Outline each blood parasite and name the species.
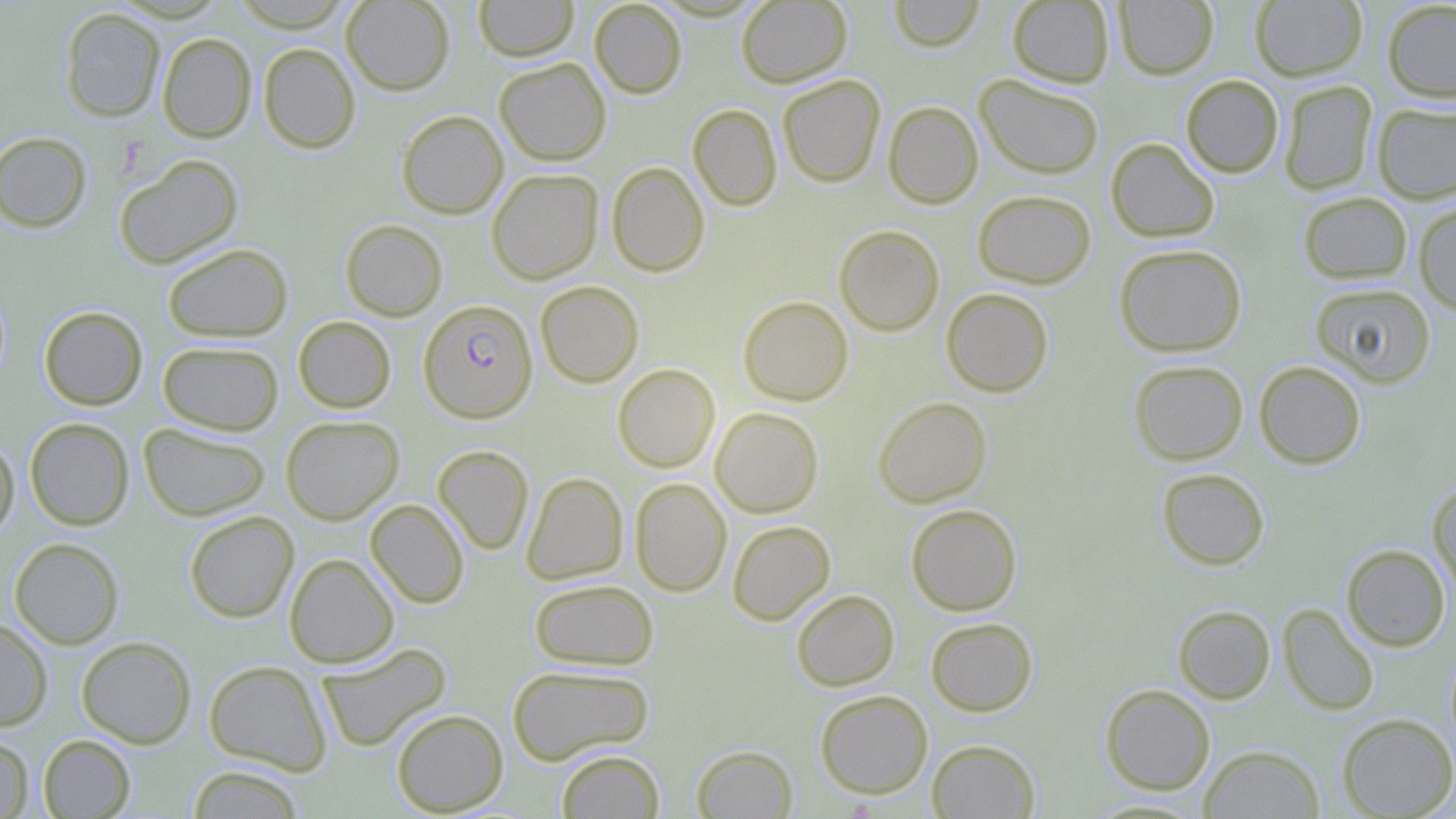

Approximate bounding boxes as named x1/y1/x2/y2 corners in pixels.
Plasmodium falciparum-infected red blood cells: (x1=418, y1=299, x2=537, y2=422).
No Plasmodium ovale, Plasmodium malariae, Plasmodium vivax, Babesia divergens, or Trypanosoma brucei observed.

Uninfected red blood cell locations: (x1=341, y1=0, x2=455, y2=95), (x1=474, y1=0, x2=579, y2=61), (x1=589, y1=0, x2=687, y2=98), (x1=736, y1=0, x2=852, y2=88), (x1=888, y1=0, x2=986, y2=52), (x1=1007, y1=0, x2=1114, y2=88), (x1=1114, y1=0, x2=1219, y2=79), (x1=1250, y1=0, x2=1367, y2=81), (x1=1381, y1=1, x2=1456, y2=103), (x1=60, y1=7, x2=165, y2=122), (x1=157, y1=33, x2=256, y2=142), (x1=259, y1=43, x2=360, y2=153), (x1=494, y1=57, x2=611, y2=165), (x1=974, y1=73, x2=1105, y2=179), (x1=777, y1=74, x2=885, y2=187), (x1=1181, y1=74, x2=1284, y2=177), (x1=1278, y1=80, x2=1378, y2=195), (x1=883, y1=101, x2=983, y2=209), (x1=1372, y1=102, x2=1456, y2=204), (x1=688, y1=104, x2=782, y2=211), (x1=396, y1=110, x2=508, y2=218), (x1=0, y1=131, x2=92, y2=233), (x1=1105, y1=137, x2=1220, y2=242), (x1=114, y1=154, x2=243, y2=269), (x1=606, y1=161, x2=709, y2=276), (x1=486, y1=168, x2=603, y2=284), (x1=972, y1=189, x2=1096, y2=288), (x1=1297, y1=191, x2=1413, y2=285), (x1=1413, y1=201, x2=1456, y2=315), (x1=340, y1=219, x2=447, y2=320), (x1=834, y1=225, x2=944, y2=336), (x1=162, y1=243, x2=293, y2=342), (x1=1114, y1=243, x2=1247, y2=356), (x1=535, y1=280, x2=644, y2=387), (x1=1309, y1=282, x2=1437, y2=388), (x1=940, y1=287, x2=1054, y2=397), (x1=738, y1=296, x2=853, y2=405), (x1=39, y1=306, x2=148, y2=410), (x1=293, y1=316, x2=396, y2=413), (x1=157, y1=341, x2=284, y2=436), (x1=1128, y1=360, x2=1248, y2=465), (x1=1254, y1=361, x2=1367, y2=469), (x1=612, y1=363, x2=720, y2=472), (x1=872, y1=396, x2=992, y2=507), (x1=710, y1=407, x2=824, y2=517), (x1=280, y1=415, x2=404, y2=524), (x1=25, y1=417, x2=134, y2=530), (x1=138, y1=422, x2=271, y2=521), (x1=0, y1=435, x2=19, y2=543), (x1=432, y1=445, x2=533, y2=555), (x1=1156, y1=468, x2=1270, y2=570), (x1=521, y1=471, x2=629, y2=585), (x1=630, y1=478, x2=731, y2=597), (x1=1427, y1=480, x2=1456, y2=595), (x1=366, y1=499, x2=469, y2=608), (x1=905, y1=504, x2=1022, y2=616), (x1=183, y1=510, x2=299, y2=622), (x1=727, y1=520, x2=836, y2=625), (x1=9, y1=538, x2=124, y2=649), (x1=1341, y1=544, x2=1451, y2=652), (x1=284, y1=553, x2=399, y2=668), (x1=529, y1=578, x2=659, y2=671), (x1=791, y1=590, x2=899, y2=691), (x1=1278, y1=603, x2=1379, y2=716), (x1=1172, y1=605, x2=1276, y2=704), (x1=925, y1=616, x2=1038, y2=717), (x1=0, y1=617, x2=52, y2=730), (x1=77, y1=636, x2=196, y2=748), (x1=318, y1=642, x2=451, y2=751), (x1=204, y1=659, x2=332, y2=775), (x1=506, y1=664, x2=655, y2=765), (x1=1100, y1=684, x2=1215, y2=795), (x1=815, y1=689, x2=933, y2=798), (x1=391, y1=708, x2=508, y2=816), (x1=1337, y1=713, x2=1456, y2=818), (x1=38, y1=734, x2=135, y2=818), (x1=0, y1=735, x2=34, y2=818), (x1=927, y1=739, x2=1041, y2=818), (x1=691, y1=744, x2=799, y2=818), (x1=1199, y1=744, x2=1325, y2=818), (x1=556, y1=749, x2=665, y2=818), (x1=186, y1=765, x2=305, y2=818), (x1=1085, y1=798, x2=1210, y2=818). Slide-level diagnosis: Plasmodium falciparum. May-Grünwald-Giemsa-stained preparation. Thin blood smear. Optical microscopy. 1000x magnification. Image is 1456×819 pixels. Single field of view.